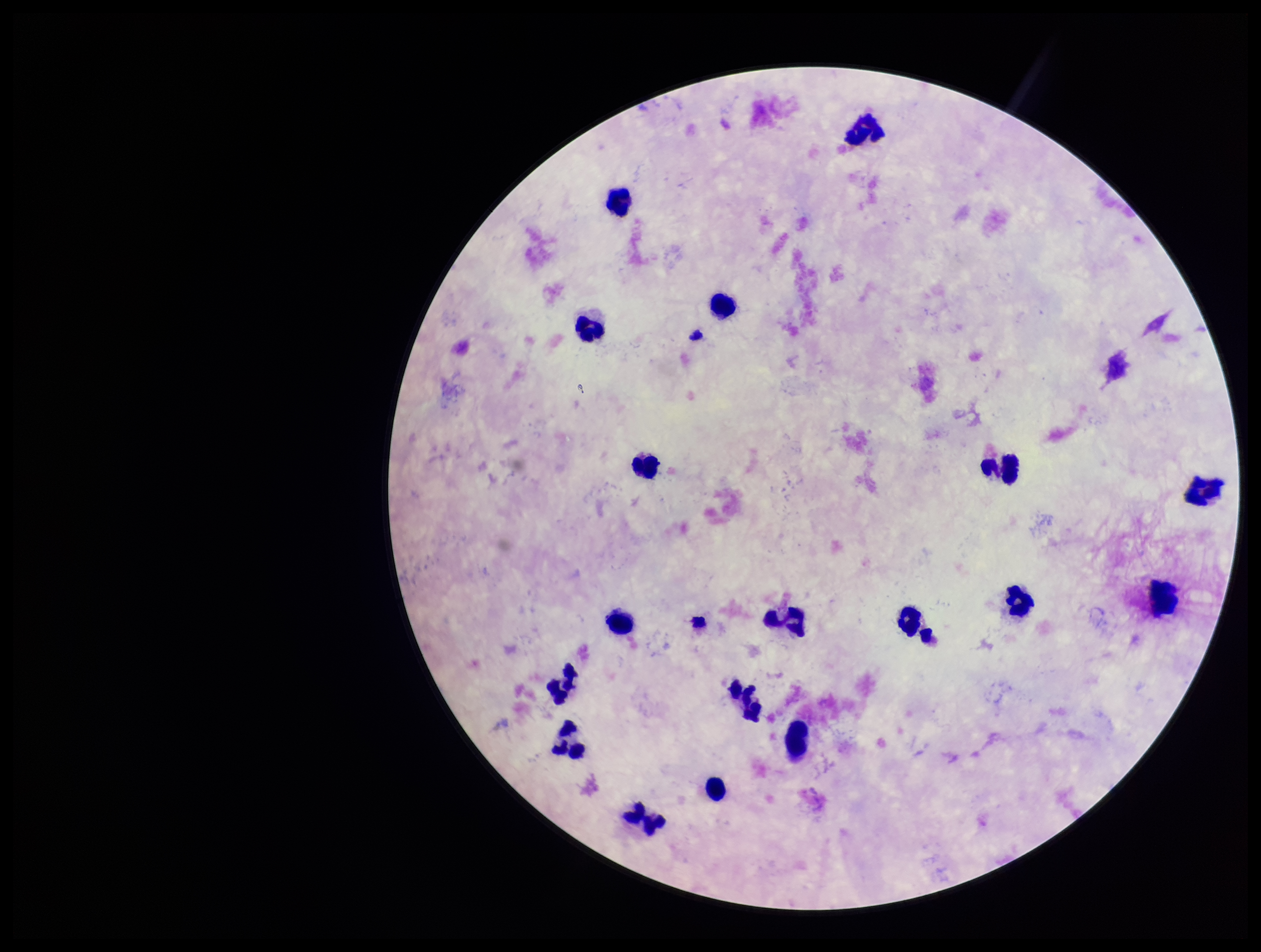

stain = Giemsa
image size = 1261×952 pixels
patient malaria status = negative
capture = smartphone photograph through the microscope eyepiece
preparation = thick smear
leukocyte count = 18
parasite count = 0
field of view = single
Plasmodium parasites = none seen